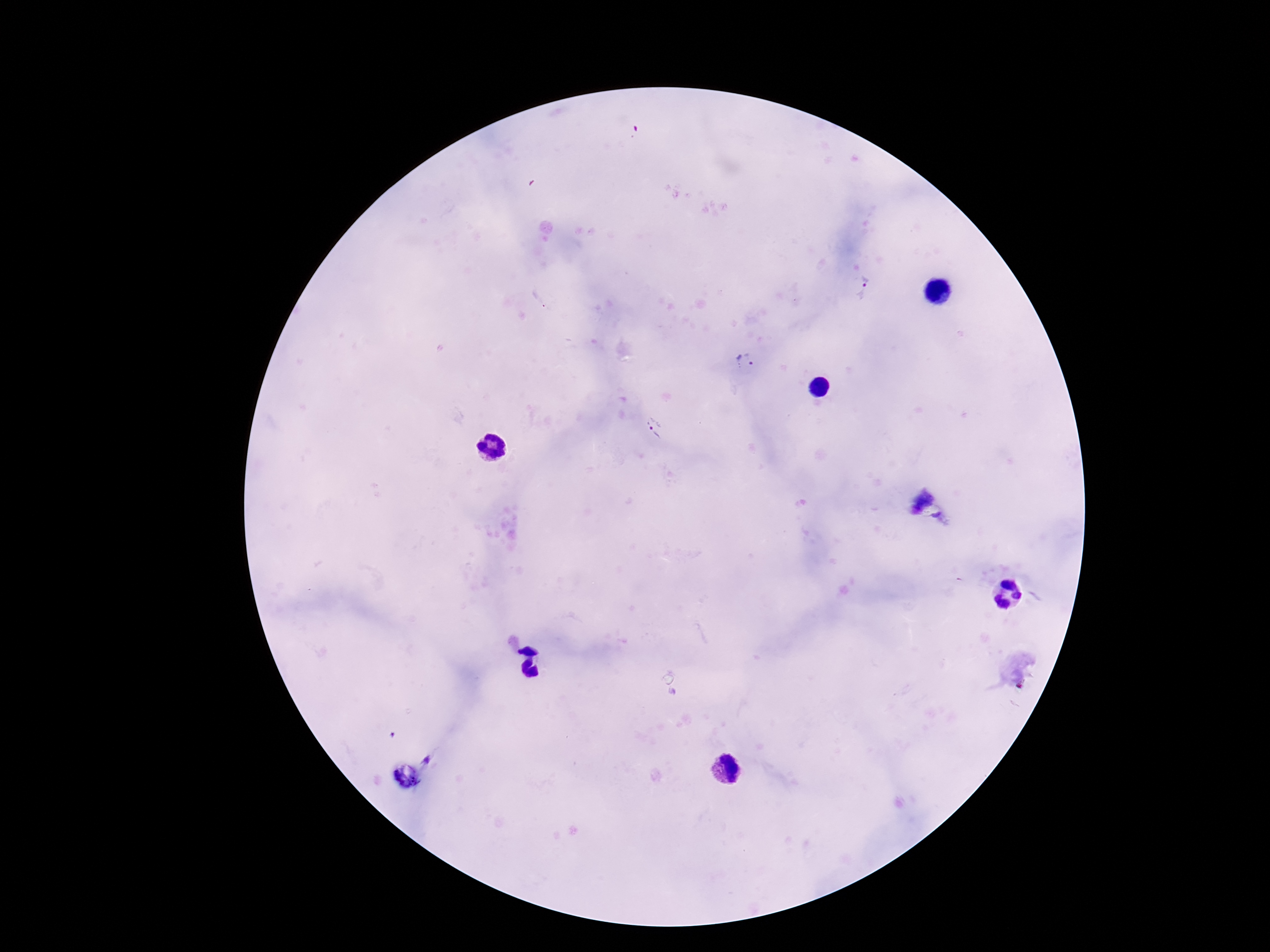

magnification = 100x
stain = Giemsa
field of view = single
image size = 1270×952 pixels
Plasmodium parasite locations = approximate centers as (x, y) in pixels: (864, 288), (744, 361), (655, 428)
patient malaria status = infected
capture = smartphone camera through the microscope eyepiece
preparation = thick blood smear